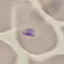
Summary:
  - Result: no malaria parasites detected
  - Preparation: thin blood smear
  - Stain: Giemsa
  - Capture: smartphone camera at the microscope eyepiece
  - Image type: cell patch, automatically extracted from a larger field of view and resized to 64 × 64 pixels